State which parasite is depicted.
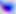

Toxoplasma gondii.

Summary:
  - Modality: micrograph
  - Magnification: 400x